Identify the blood parasite species.
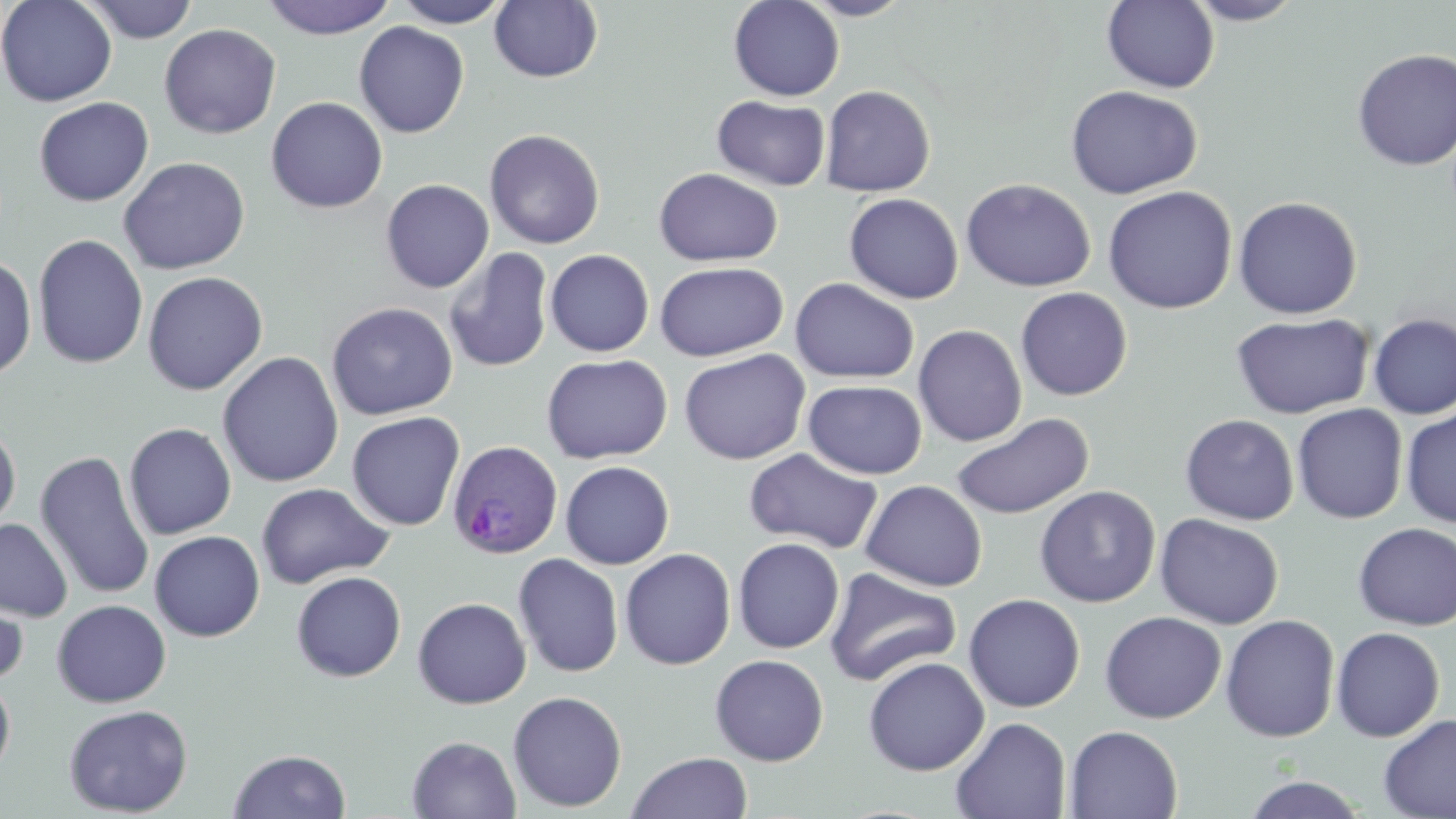

Plasmodium ovale.

image size = 1456×819 pixels
field of view = one of a larger specimen
stain = May-Grünwald-Giemsa
Plasmodium ovale-infected red blood cell locations = approximate bounding boxes as [x1, y1, x2, y2] in pixels: [447, 440, 562, 559]
preparation = thin blood smear
magnification = 1000x
modality = light microscopy
uninfected red blood cell locations = approximate bounding boxes as [x1, y1, x2, y2] in pixels: [1, 0, 118, 107], [79, 0, 200, 44], [260, 0, 398, 40], [392, 0, 513, 28], [728, 0, 845, 101], [797, 0, 916, 20], [489, 1, 603, 83], [1101, 1, 1220, 93], [1184, 1, 1305, 25], [353, 22, 470, 138], [159, 23, 281, 139], [1351, 48, 1456, 171], [820, 85, 936, 197], [1065, 85, 1202, 199], [266, 96, 388, 214], [712, 96, 830, 191], [34, 97, 154, 206], [484, 129, 605, 250], [118, 156, 250, 274], [653, 168, 784, 267], [961, 178, 1096, 292], [380, 179, 494, 294], [1102, 185, 1238, 314], [843, 193, 964, 304], [1232, 196, 1363, 319], [32, 233, 148, 370], [443, 248, 554, 373], [545, 250, 654, 357], [0, 254, 37, 383], [654, 261, 789, 362], [142, 271, 268, 395], [790, 278, 919, 384], [1015, 287, 1133, 401], [326, 302, 458, 421], [1230, 312, 1374, 419], [1368, 313, 1456, 419], [913, 324, 1027, 446], [678, 348, 811, 465], [217, 351, 344, 488], [541, 353, 673, 464], [803, 380, 927, 479], [1292, 403, 1408, 523], [1401, 407, 1456, 527], [346, 411, 465, 531], [951, 412, 1094, 519], [1180, 414, 1300, 525], [0, 420, 21, 536], [124, 422, 236, 540], [745, 448, 884, 554], [34, 449, 155, 601], [560, 461, 674, 569], [860, 479, 988, 592], [255, 482, 393, 589], [1034, 485, 1161, 608], [1155, 513, 1284, 630], [0, 517, 73, 623], [1353, 522, 1456, 631], [149, 530, 265, 642], [732, 537, 844, 654], [620, 548, 736, 670], [513, 553, 624, 677], [824, 567, 961, 687], [291, 571, 407, 682], [0, 584, 29, 688], [963, 593, 1086, 712], [412, 597, 531, 709], [52, 599, 171, 707], [1100, 611, 1226, 723], [1220, 614, 1340, 743], [1331, 626, 1445, 742], [710, 654, 829, 766], [863, 657, 989, 776], [0, 674, 16, 782], [507, 690, 628, 812], [63, 704, 193, 817], [1378, 712, 1456, 819], [950, 716, 1071, 819], [1064, 725, 1183, 818], [407, 735, 521, 819], [228, 749, 351, 818], [626, 752, 753, 819], [1239, 775, 1371, 818]